Give the position of every Plasmodium parasite.
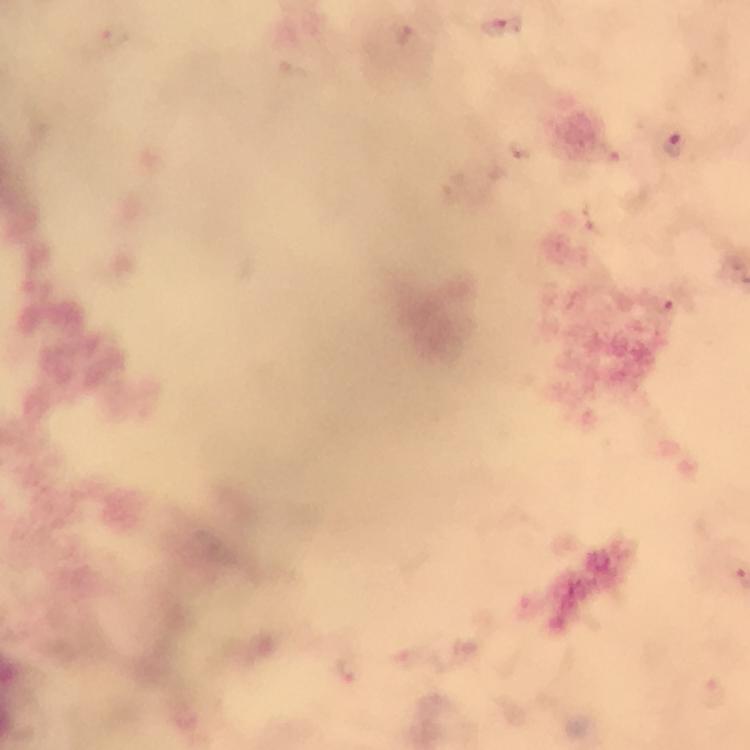

Approximate centers as (x, y) in pixels.
Plasmodium parasites: (503, 26), (116, 34), (675, 143), (665, 308), (350, 669), (716, 692).

magnification = 100x
stain = Giemsa
cropped from = a single field of view
immersion oil = applied
capture = smartphone camera through the microscope
preparation = thick blood film
context = from a malaria diagnostic workup
image size = 750×750 pixels